Report the malaria status of this cell.
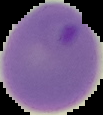

Parasitized.

The area outside the segmented cell region is set to black. Image is 103×115 pixels. From a thin blood film.